Locate and identify every blood parasite.
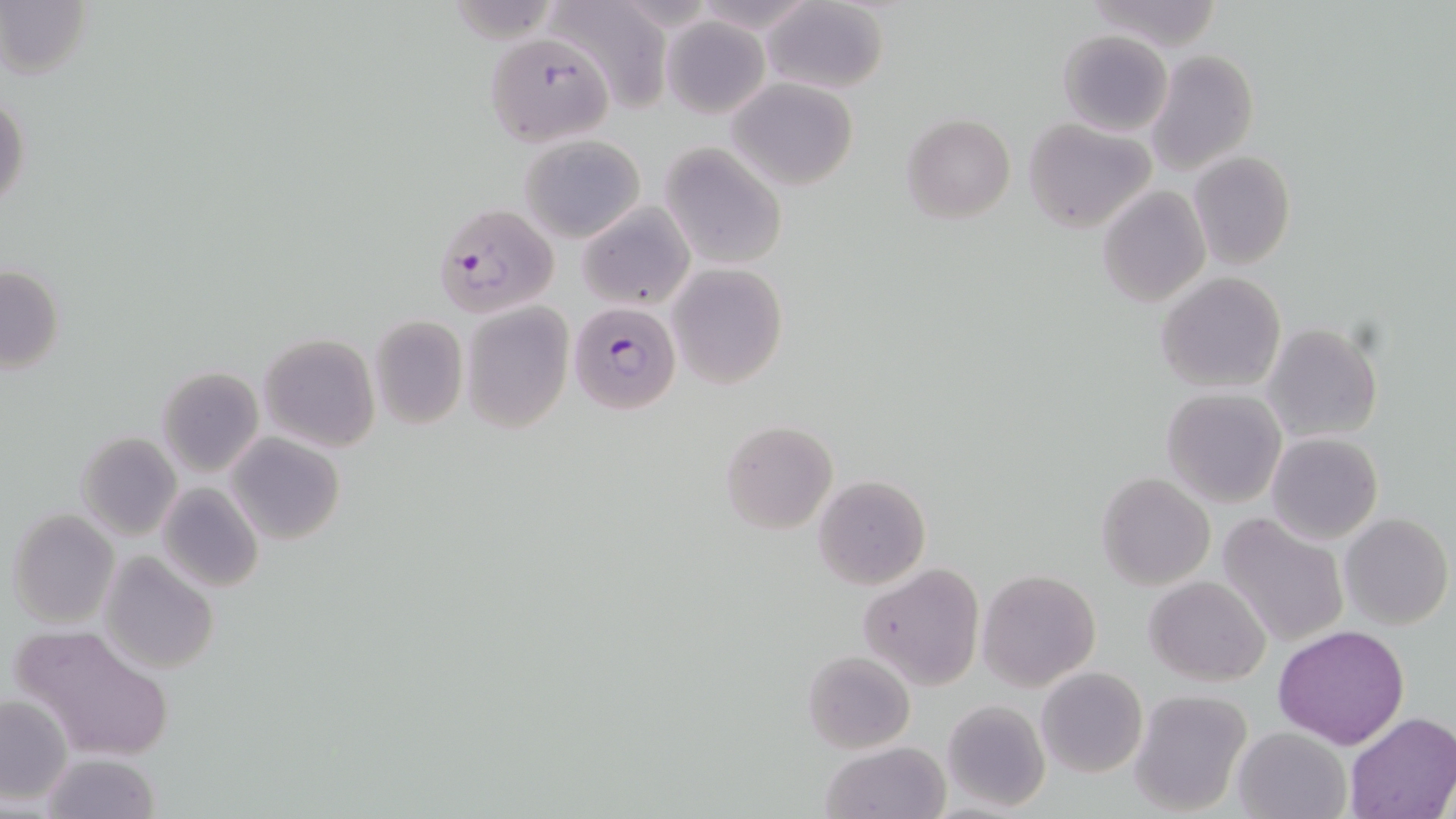
Approximate bounding boxes as (x1,y1)-(x2,y2) corner pairs in pixels.
Plasmodium falciparum-infected red blood cells: (433,202)-(558,318), (569,302)-(682,416).
No Plasmodium ovale, Plasmodium malariae, Plasmodium vivax, Babesia divergens, or Trypanosoma brucei observed.

Summary:
  - Uninfected red blood cell locations: (760,0)-(889,95), (1,1)-(89,82), (546,1)-(669,110), (1085,1)-(1221,50), (661,16)-(769,119), (1058,29)-(1172,137), (484,32)-(614,146), (1144,49)-(1259,174), (726,78)-(859,190), (1,90)-(31,213), (901,113)-(1015,224), (1023,119)-(1157,233), (520,134)-(646,242), (658,144)-(788,270), (1189,151)-(1295,272), (1098,185)-(1210,309), (577,200)-(694,310), (668,262)-(787,390), (2,263)-(65,376), (1155,273)-(1286,394), (461,302)-(574,433), (368,316)-(468,428), (1263,323)-(1382,445), (260,334)-(380,453), (156,366)-(264,475), (1161,387)-(1286,507), (720,421)-(837,536), (77,431)-(183,542), (1266,431)-(1382,544), (226,434)-(345,544), (1097,473)-(1214,590), (812,475)-(930,590), (156,482)-(265,595), (7,509)-(119,628), (1217,512)-(1349,646), (1340,513)-(1452,629), (100,550)-(219,676), (858,563)-(985,690), (977,569)-(1100,690), (1144,575)-(1271,685), (11,624)-(174,764), (1273,625)-(1410,748), (804,650)-(914,754), (1035,666)-(1148,778), (1128,690)-(1249,815), (0,695)-(72,803), (941,699)-(1050,813), (1342,712)-(1455,819), (1233,727)-(1349,819), (821,741)-(950,819), (40,752)-(158,819)
  - Slide-level diagnosis: Plasmodium falciparum
  - Magnification: 1000x
  - Image size: 1456×819 pixels
  - Preparation: thin blood smear
  - Field of view: single
  - Modality: optical microscopy
  - Stain: May-Grünwald-Giemsa